State which parasite is depicted.
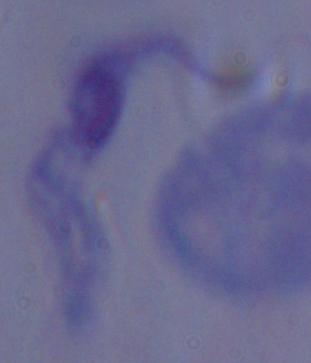
This is a trypanosome.

Summary:
  - Modality: photomicrograph
  - Magnification: 1000x